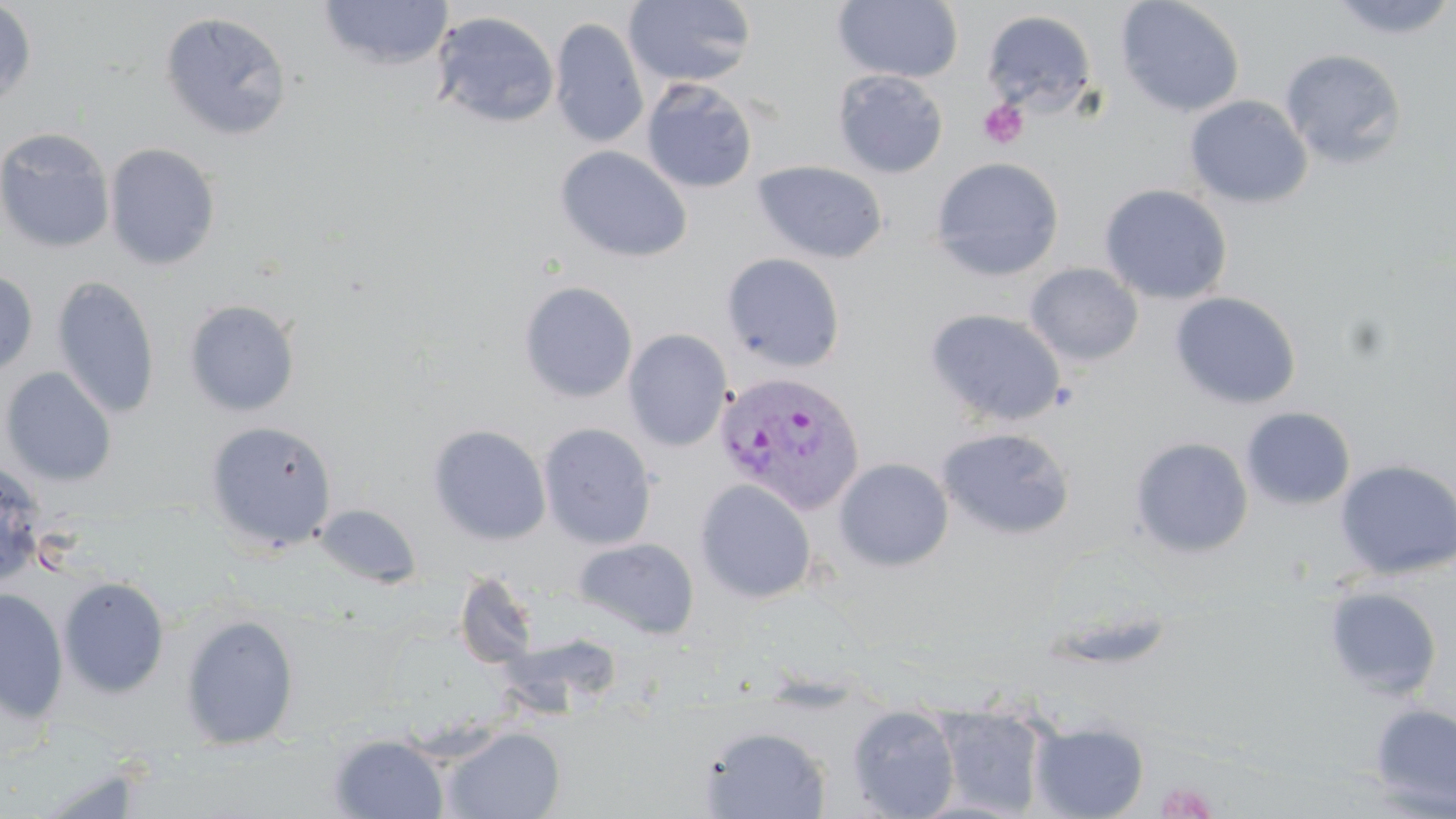

Approximate bounding boxes as (x1, y1, x2, y2) in pixels. Platelet locations: (978, 99, 1028, 149), (1159, 781, 1218, 818). Uninfected red blood cell locations: (318, 0, 453, 69), (623, 0, 758, 88), (832, 0, 964, 83), (1115, 0, 1246, 117), (1328, 0, 1456, 41), (0, 1, 36, 110), (982, 9, 1098, 119), (429, 10, 560, 128), (159, 11, 293, 141), (550, 17, 649, 149), (1280, 49, 1408, 168), (832, 69, 948, 178), (641, 78, 759, 194), (1185, 95, 1312, 209), (0, 128, 114, 253), (104, 142, 221, 270), (555, 145, 693, 263), (931, 157, 1065, 281), (752, 160, 888, 264), (1099, 184, 1232, 305), (721, 252, 846, 372), (1025, 263, 1143, 366), (0, 269, 38, 379), (52, 276, 161, 419), (518, 280, 639, 403), (1170, 292, 1302, 410), (184, 299, 301, 417), (926, 308, 1066, 427), (623, 329, 732, 451), (1, 367, 117, 486), (1240, 407, 1356, 510), (204, 419, 338, 554), (427, 423, 551, 545), (538, 423, 657, 550), (937, 427, 1075, 540), (1130, 437, 1254, 558), (833, 457, 954, 572), (1335, 459, 1456, 580), (0, 460, 47, 590), (695, 479, 817, 604), (314, 504, 421, 588), (572, 537, 700, 639), (455, 570, 540, 669), (58, 576, 170, 698), (1323, 586, 1443, 700), (1, 587, 69, 724), (180, 614, 300, 750), (1369, 703, 1456, 816), (847, 705, 961, 818), (936, 707, 1047, 817), (1030, 722, 1149, 819), (441, 726, 565, 818), (701, 726, 830, 817), (329, 734, 449, 818). Plasmodium vivax-infected red blood cell locations: (714, 371, 867, 516). Slide-level diagnosis: Plasmodium vivax. May-Grünwald-Giemsa stain. Image is 1456×819 pixels. Optical microscopy. Thin blood film. One field of a larger specimen. 1000x magnification.